Assess this cell for malaria.
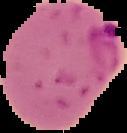
It is parasitized.

Summary:
  - Image size: 127×133 pixels
  - Preparation: thin blood film
  - Image type: segmented cell region on a black background